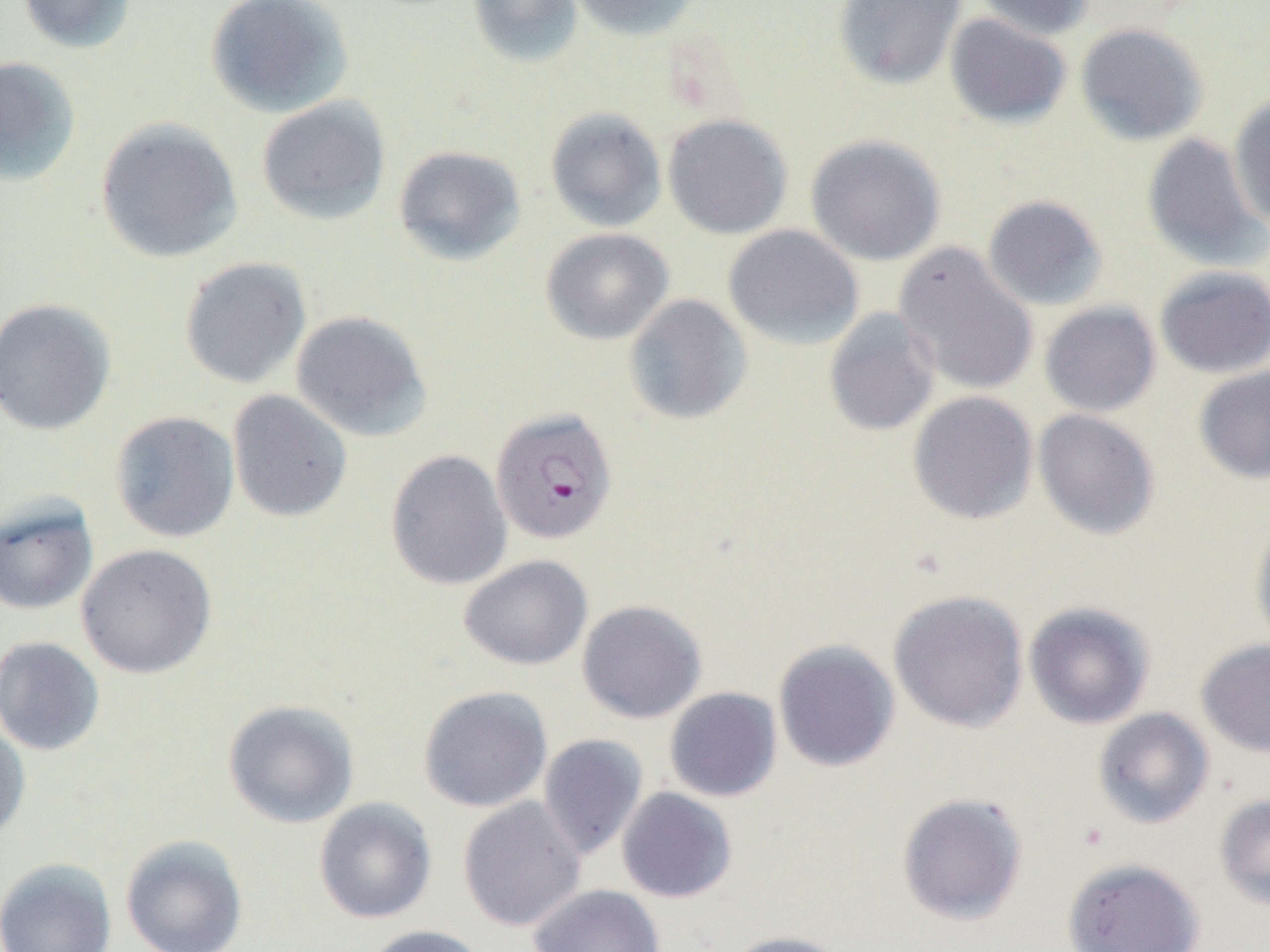
slide_level_diagnosis: Plasmodium falciparum
magnification: 1000x
field_of_view: single
image_size: 1270×952 pixels
modality: optical microscopy
plasmodium_falciparum_infected_red_blood_cell_locations: 'approximate bounding boxes as (x1,y1)-(x2,y2) corner pairs in pixels: (490,407)-(617,544)'
preparation: thin blood film
uninfected_red_blood_cell_locations: 'approximate bounding boxes as (x1,y1)-(x2,y2) corner pairs in pixels: (16,0)-(137,54), (205,0)-(353,119), (468,0)-(583,68), (569,0)-(702,41), (833,0)-(967,89), (973,0)-(1095,40), (944,13)-(1072,128), (1075,22)-(1209,146), (0,55)-(81,187), (1229,93)-(1270,229), (256,95)-(391,226), (544,106)-(668,233), (662,113)-(793,239), (94,117)-(243,264), (1142,132)-(1268,272), (805,134)-(946,266), (393,145)-(526,266), (982,195)-(1108,312), (723,224)-(863,350), (541,228)-(674,345), (893,242)-(1039,397), (178,256)-(312,389), (1155,265)-(1270,378), (623,294)-(753,426), (0,297)-(117,436), (1039,301)-(1161,417), (822,308)-(941,437), (290,310)-(432,442), (1193,364)-(1270,485), (227,390)-(353,522), (908,391)-(1039,525), (1032,408)-(1160,541), (109,411)-(240,543), (385,449)-(513,591), (0,496)-(99,616), (1249,515)-(1270,653), (76,543)-(217,679), (459,555)-(593,670), (888,589)-(1029,733), (576,599)-(707,724), (1023,601)-(1156,730), (0,636)-(105,756), (1195,638)-(1270,758), (773,640)-(901,772), (418,685)-(552,813), (664,687)-(782,802), (222,699)-(360,828), (1092,707)-(1214,829), (0,715)-(31,846), (538,734)-(649,860), (616,787)-(738,903), (896,791)-(1028,926), (1214,794)-(1270,911), (458,796)-(586,931), (313,797)-(437,924), (120,834)-(248,951), (1062,857)-(1205,952), (0,858)-(117,952), (528,884)-(666,952), (360,924)-(489,952), (720,930)-(850,952)'